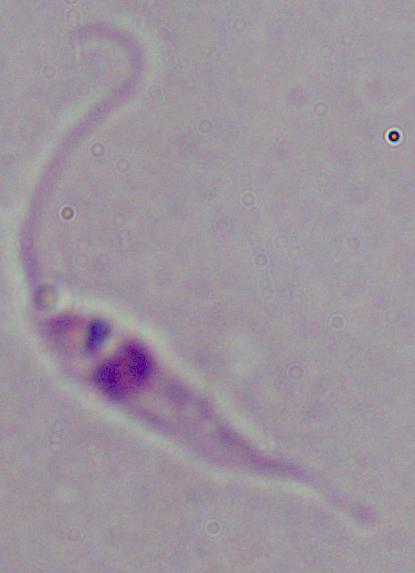
magnification = 1000x
modality = micrograph
identification = Leishmania